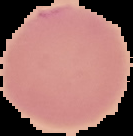

image type = segmented cell region on a black background
malaria status = uninfected
preparation = thin blood film
image size = 133×136 pixels